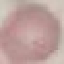
Summary:
  - Malaria status: uninfected
  - Image type: cell patch, automatically extracted from a larger field of view and resized to 64 × 64 pixels
  - Capture: smartphone through the microscope eyepiece
  - Preparation: thin blood film
  - Stain: Giemsa